Comment on the morphology of the red blood cells.
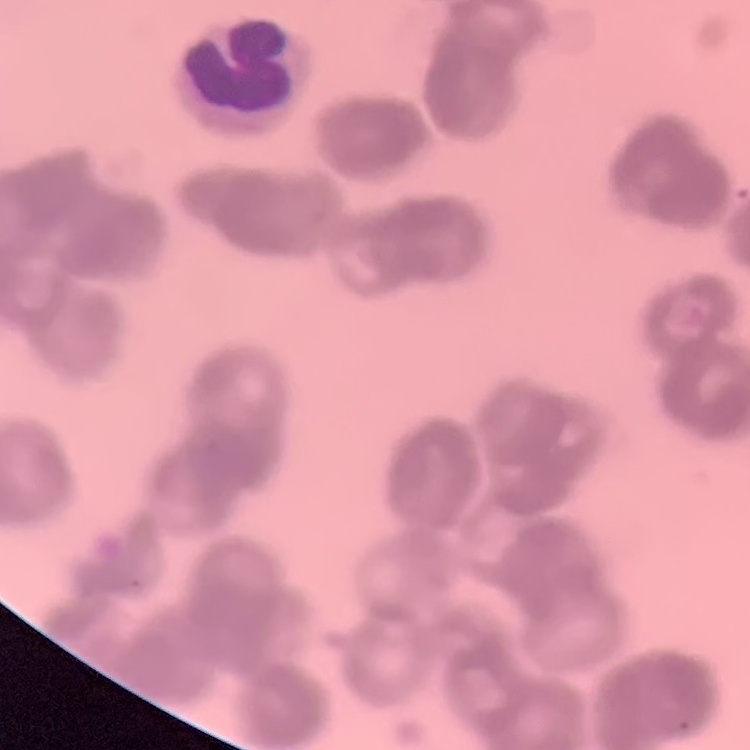

Rouleaux formation.

Summary:
  - Stain: Field's or Giemsa
  - Preparation: thin blood film
  - Image type: square crop of a larger photomicrograph